Assess this cell for malaria.
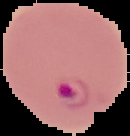

Parasitized.

Summary:
  - Image size: 130×136 pixels
  - Preparation: thin blood film
  - Image type: segmented cell region with the area outside set to black